Locate every uninfected red blood cell.
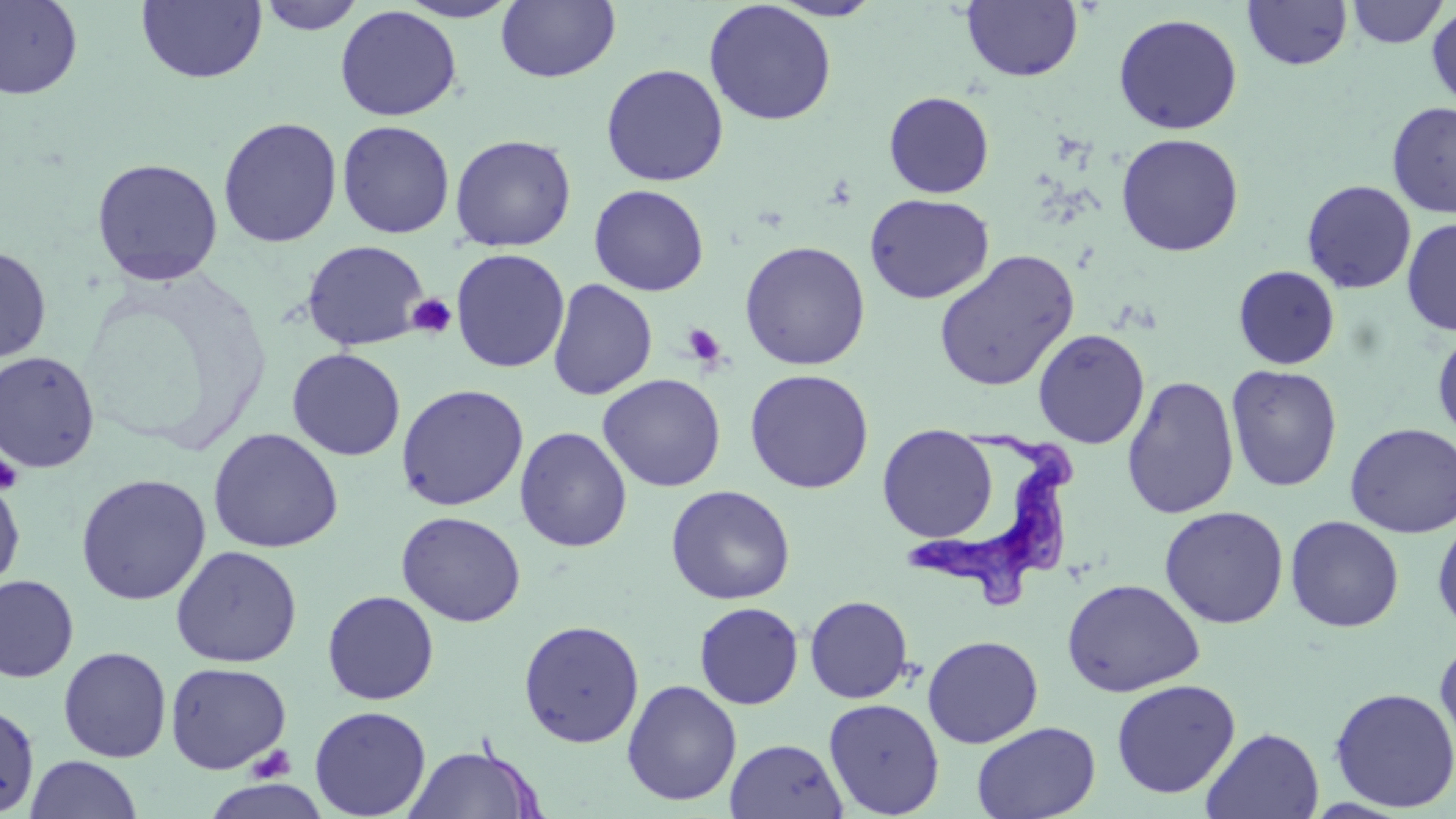

Approximate bounding boxes as [x1, y1, x2, y2] in pixels.
Uninfected red blood cells: [0, 0, 84, 100], [136, 0, 267, 84], [256, 0, 366, 35], [395, 0, 523, 22], [768, 0, 885, 21], [495, 1, 621, 83], [962, 1, 1083, 82], [1243, 1, 1352, 70], [1346, 1, 1447, 48], [703, 2, 836, 126], [335, 5, 462, 121], [1426, 6, 1456, 111], [1112, 13, 1243, 135], [601, 63, 728, 187], [884, 91, 994, 198], [1387, 101, 1456, 218], [217, 117, 342, 249], [336, 120, 456, 239], [1115, 132, 1244, 257], [450, 134, 576, 252], [91, 157, 224, 287], [1301, 180, 1417, 294], [588, 184, 709, 296], [864, 193, 994, 304], [1402, 218, 1456, 337], [301, 239, 429, 351], [739, 240, 871, 370], [0, 245, 52, 365], [450, 248, 570, 373], [933, 249, 1080, 392], [1233, 265, 1340, 370], [547, 279, 658, 401], [1432, 326, 1456, 444], [1032, 328, 1150, 449], [287, 348, 406, 461], [0, 351, 101, 473], [1225, 364, 1343, 492], [744, 368, 874, 493], [597, 373, 726, 492], [1121, 375, 1240, 520], [395, 383, 529, 511], [1345, 422, 1456, 538], [878, 424, 998, 542], [514, 426, 632, 552], [207, 428, 344, 554], [75, 473, 211, 605], [0, 478, 25, 595], [665, 484, 796, 605], [1159, 505, 1289, 629], [396, 511, 526, 627], [1432, 511, 1456, 638], [1285, 515, 1404, 632], [169, 545, 303, 668], [0, 574, 80, 683], [1061, 578, 1205, 697], [322, 590, 440, 705], [805, 595, 913, 703], [694, 602, 804, 710], [518, 620, 645, 747], [922, 634, 1043, 748], [1434, 635, 1456, 761], [58, 646, 172, 762], [165, 661, 291, 774], [1111, 678, 1241, 798], [622, 679, 742, 805], [1329, 687, 1456, 812], [823, 697, 944, 817], [0, 700, 40, 818], [309, 705, 432, 819], [971, 721, 1101, 819], [1201, 727, 1324, 819], [725, 737, 848, 819], [404, 743, 544, 819], [25, 754, 142, 818].

{
  "slide_level_diagnosis": "Trypanosoma brucei",
  "platelet_locations": "approximate bounding boxes as [x1, y1, x2, y2] in pixels: [408, 294, 457, 339], [681, 323, 727, 368], [0, 455, 24, 494], [249, 743, 296, 783]",
  "trypanosoma_brucei_locations": "approximate bounding boxes as [x1, y1, x2, y2] in pixels: [908, 420, 1080, 610]",
  "magnification": "1000x",
  "field_of_view": "one of a larger specimen",
  "image_size": "1456×819 pixels",
  "preparation": "thin blood film",
  "modality": "optical microscopy",
  "stain": "May-Grünwald-Giemsa"
}